Report the malaria status of this cell.
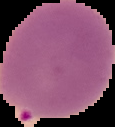

It is parasitized.

{
  "image_size": "115×127 pixels",
  "preparation": "thin blood smear",
  "image_type": "segmented cell region with the area outside set to black"
}